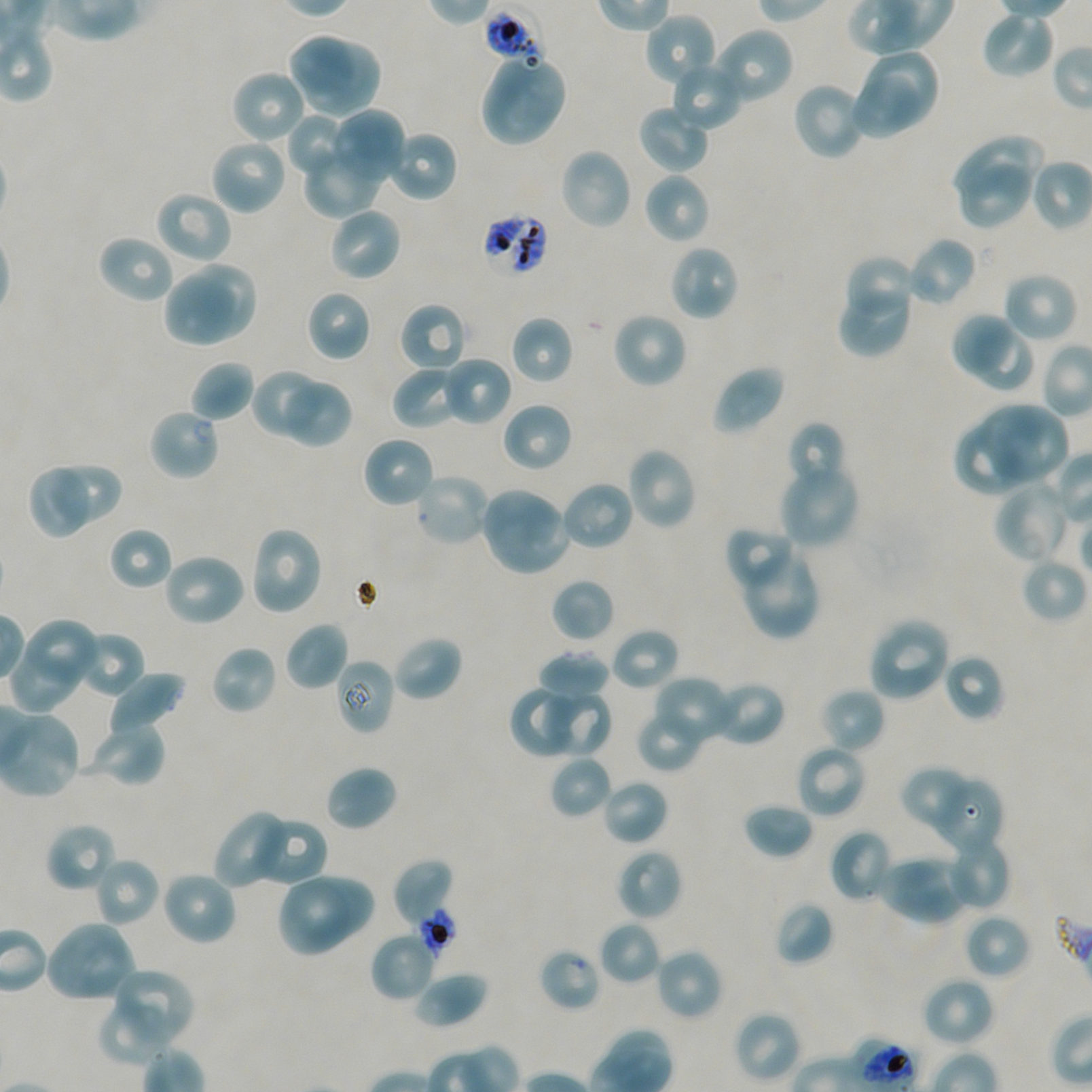

Approximate bounding boxes as (x1, y1, x2, y2) in pixels. Not every red blood cell is marked. Locations of red blood cells of indeterminate infection status: (484, 10, 546, 67), (481, 212, 549, 277), (414, 907, 458, 958), (539, 947, 602, 1012), (850, 1037, 917, 1092). Locations of uninfected red blood cells: (982, 10, 1055, 79), (644, 12, 717, 90), (711, 26, 795, 107), (287, 32, 359, 98), (298, 43, 380, 115), (865, 50, 938, 124), (479, 52, 568, 147), (671, 60, 744, 131), (230, 70, 308, 145), (849, 74, 924, 139), (791, 80, 868, 161), (638, 103, 711, 174), (327, 109, 405, 187), (287, 113, 353, 179), (387, 129, 458, 203), (209, 138, 288, 216), (953, 139, 1042, 196), (304, 141, 385, 217), (558, 147, 633, 231), (959, 162, 1032, 227), (643, 172, 711, 244), (153, 190, 233, 265), (327, 206, 403, 283), (97, 234, 176, 304), (906, 236, 978, 307), (668, 244, 739, 322), (843, 254, 917, 325), (184, 263, 257, 338), (1001, 271, 1079, 343), (162, 272, 236, 348), (838, 283, 912, 357), (306, 289, 372, 362), (398, 302, 469, 374), (611, 311, 689, 389), (949, 311, 1011, 373), (511, 316, 573, 384), (968, 329, 1036, 393), (442, 355, 513, 426), (189, 360, 253, 422), (392, 365, 465, 429), (712, 365, 786, 435), (251, 368, 327, 436), (280, 378, 352, 448), (501, 402, 573, 472), (983, 404, 1072, 479), (148, 407, 221, 481), (786, 421, 848, 490), (954, 425, 1023, 497), (361, 435, 435, 510), (625, 446, 698, 530), (30, 462, 91, 541), (778, 462, 861, 550), (54, 467, 122, 523), (413, 471, 492, 547), (992, 478, 1072, 564), (560, 479, 636, 551), (479, 486, 571, 577), (249, 525, 324, 616), (109, 526, 173, 591), (722, 526, 799, 598), (744, 547, 821, 640), (162, 551, 247, 627), (1020, 557, 1087, 624), (551, 578, 615, 642), (867, 617, 951, 703), (285, 621, 349, 691), (26, 623, 98, 682), (609, 627, 681, 692), (73, 630, 145, 699), (393, 635, 463, 702), (210, 644, 278, 716), (8, 651, 83, 716), (538, 651, 611, 699), (942, 653, 1006, 722), (335, 658, 395, 736), (106, 670, 187, 735), (651, 675, 737, 750), (708, 680, 786, 746), (509, 686, 586, 759), (538, 687, 612, 757), (818, 687, 886, 754), (636, 706, 706, 772), (0, 707, 77, 799), (88, 721, 166, 786), (795, 742, 867, 820), (549, 755, 613, 819), (324, 764, 398, 831), (899, 766, 977, 832), (929, 776, 1004, 857), (601, 778, 668, 846), (742, 802, 814, 859), (213, 809, 294, 889), (251, 816, 328, 888), (45, 822, 117, 893), (829, 829, 894, 903), (945, 833, 1012, 911), (616, 848, 682, 922), (92, 856, 160, 927), (911, 856, 972, 915), (393, 857, 454, 927), (879, 861, 959, 926), (160, 871, 238, 947), (287, 875, 375, 943), (275, 881, 350, 959), (774, 901, 834, 966), (964, 913, 1031, 979), (43, 920, 136, 1004), (598, 920, 662, 985), (371, 930, 438, 1002), (655, 948, 723, 1021), (115, 967, 196, 1034), (412, 971, 488, 1029), (920, 976, 996, 1047), (96, 998, 170, 1067), (733, 1011, 802, 1084). Plasmodium falciparum strain NF54 maintained in static in-vitro culture. Blood group of the donor: A+/O+. 100x objective under oil immersion, numerical aperture 1.45. Image is 1092×1092 pixels. Giemsa stain. Thin blood film. One field from this slide.